Classify this cell by malaria status.
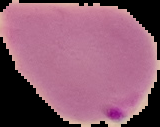
Parasitized.

Cell region segmented out of the field of view; the surrounding area is masked to black. From a thin blood film. Image is 160×127 pixels.